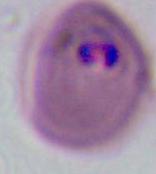 A Plasmodium parasite is seen. Captured at either 400x or 1000x magnification. Micrograph.